Classify this cell by malaria status.
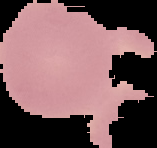
Uninfected.

Summary:
  - Preparation: thin blood film
  - Image size: 157×148 pixels
  - Image type: segmented cell region with the area outside set to black